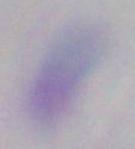

Toxoplasma gondii is seen. 1000x magnification. Photomicrograph.